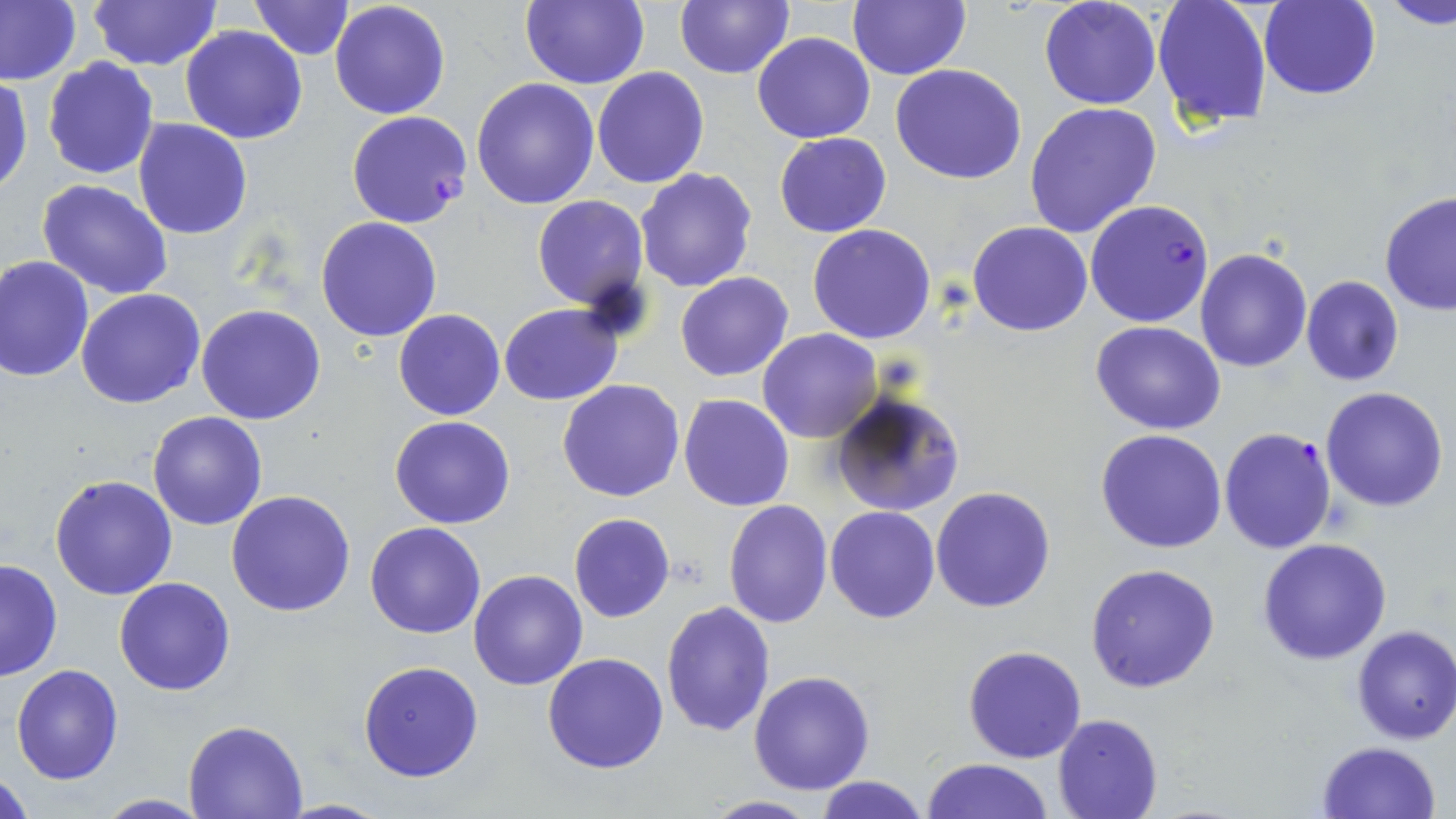
Approximate bounding boxes as named x1/y1/x2/y2 corners in pixels. Plasmodium falciparum-infected red blood cell locations: (x1=346, y1=110, x2=472, y2=228), (x1=1085, y1=199, x2=1214, y2=328), (x1=1219, y1=425, x2=1338, y2=555). Uninfected red blood cell locations: (x1=1, y1=0, x2=81, y2=87), (x1=88, y1=0, x2=222, y2=71), (x1=248, y1=0, x2=354, y2=60), (x1=520, y1=0, x2=649, y2=89), (x1=675, y1=0, x2=793, y2=79), (x1=848, y1=0, x2=970, y2=81), (x1=1039, y1=0, x2=1162, y2=110), (x1=1151, y1=0, x2=1272, y2=127), (x1=1379, y1=0, x2=1455, y2=28), (x1=330, y1=1, x2=451, y2=119), (x1=1259, y1=1, x2=1381, y2=100), (x1=180, y1=26, x2=308, y2=146), (x1=751, y1=31, x2=875, y2=144), (x1=42, y1=56, x2=158, y2=179), (x1=891, y1=64, x2=1026, y2=185), (x1=593, y1=67, x2=709, y2=188), (x1=0, y1=75, x2=32, y2=196), (x1=471, y1=78, x2=602, y2=210), (x1=1023, y1=101, x2=1163, y2=239), (x1=132, y1=118, x2=253, y2=239), (x1=774, y1=132, x2=891, y2=237), (x1=635, y1=168, x2=758, y2=293), (x1=37, y1=180, x2=174, y2=299), (x1=1380, y1=190, x2=1456, y2=317), (x1=531, y1=195, x2=648, y2=312), (x1=316, y1=217, x2=442, y2=341), (x1=968, y1=221, x2=1093, y2=336), (x1=807, y1=224, x2=936, y2=344), (x1=1194, y1=247, x2=1312, y2=372), (x1=0, y1=254, x2=96, y2=381), (x1=675, y1=271, x2=794, y2=381), (x1=1300, y1=275, x2=1404, y2=386), (x1=75, y1=289, x2=205, y2=409), (x1=499, y1=303, x2=623, y2=405), (x1=196, y1=304, x2=328, y2=426), (x1=394, y1=309, x2=505, y2=421), (x1=1091, y1=321, x2=1225, y2=436), (x1=758, y1=329, x2=882, y2=443), (x1=557, y1=378, x2=686, y2=503), (x1=1320, y1=386, x2=1450, y2=512), (x1=831, y1=391, x2=968, y2=517), (x1=678, y1=393, x2=794, y2=512), (x1=148, y1=411, x2=268, y2=530), (x1=391, y1=415, x2=514, y2=529), (x1=1095, y1=429, x2=1228, y2=553), (x1=49, y1=474, x2=178, y2=600), (x1=931, y1=486, x2=1055, y2=613), (x1=226, y1=489, x2=357, y2=616), (x1=723, y1=499, x2=832, y2=629), (x1=824, y1=505, x2=940, y2=623), (x1=569, y1=514, x2=675, y2=622), (x1=365, y1=521, x2=487, y2=638), (x1=1256, y1=536, x2=1392, y2=664), (x1=0, y1=557, x2=62, y2=683), (x1=1085, y1=563, x2=1221, y2=693), (x1=468, y1=569, x2=587, y2=690), (x1=114, y1=577, x2=237, y2=695), (x1=661, y1=601, x2=777, y2=738), (x1=1349, y1=625, x2=1456, y2=744), (x1=963, y1=645, x2=1087, y2=764), (x1=542, y1=652, x2=670, y2=773), (x1=357, y1=660, x2=484, y2=782), (x1=11, y1=664, x2=124, y2=784), (x1=748, y1=670, x2=875, y2=794), (x1=1053, y1=713, x2=1162, y2=819), (x1=183, y1=718, x2=309, y2=818), (x1=1315, y1=741, x2=1442, y2=819), (x1=923, y1=758, x2=1053, y2=818), (x1=1, y1=768, x2=32, y2=818), (x1=812, y1=777, x2=931, y2=819), (x1=94, y1=794, x2=213, y2=817), (x1=697, y1=795, x2=824, y2=817), (x1=276, y1=798, x2=392, y2=817). Slide-level diagnosis: Plasmodium falciparum. May-Grünwald-Giemsa-stained preparation. Image is 1456×819 pixels. Thin blood smear. Optical microscopy. Captured at 1000x magnification. Single field of view.